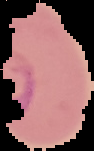

Summary:
  - Image size: 94×151 pixels
  - Image type: cell region segmented out of the field of view; surrounding area masked to black
  - Preparation: thin blood film
  - Result: malaria parasites detected